Report the malaria status of this cell.
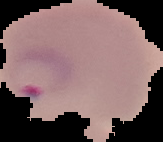

Parasitized.

Summary:
  - Image type: segmented cell region on a black background
  - Preparation: thin blood smear
  - Image size: 163×142 pixels